Locate every uninfected red blood cell.
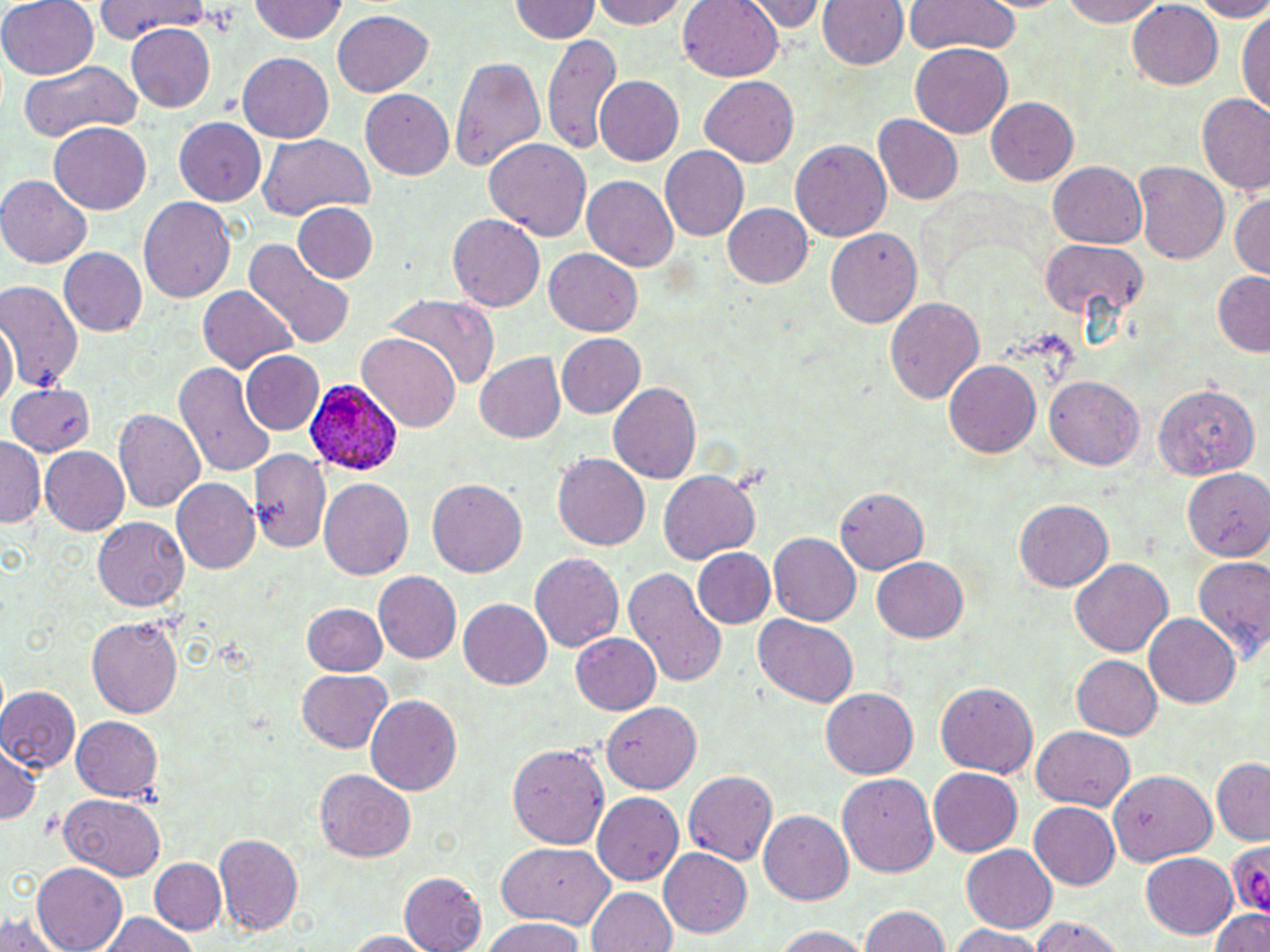

Approximate bounding boxes as (x1,y1)-(x2,y2) corner pairs in pixels.
Uninfected red blood cells: (1,0)-(99,79), (592,0)-(689,29), (678,0)-(783,81), (739,0)-(828,33), (818,0)-(907,69), (903,0)-(1020,56), (1062,0)-(1167,25), (1194,0)-(1270,21), (95,1)-(208,39), (248,1)-(349,42), (508,1)-(601,42), (1127,3)-(1223,88), (332,9)-(433,97), (1237,9)-(1269,115), (126,24)-(216,113), (544,31)-(620,155), (911,43)-(1012,137), (238,53)-(334,142), (450,54)-(545,172), (19,62)-(140,142), (596,75)-(684,165), (700,76)-(799,167), (361,89)-(453,179), (1197,93)-(1269,195), (986,97)-(1079,185), (873,114)-(963,205), (173,117)-(267,205), (50,122)-(151,213), (257,132)-(376,219), (484,138)-(590,240), (791,140)-(891,241), (659,145)-(748,242), (1048,161)-(1146,247), (1133,161)-(1228,264), (1,175)-(92,268), (582,175)-(678,271), (1230,193)-(1270,278), (138,196)-(235,302), (294,203)-(377,282), (723,204)-(813,288), (448,213)-(546,311), (825,228)-(923,328), (242,237)-(353,349), (1039,238)-(1147,319), (59,248)-(148,336), (545,249)-(642,337), (1212,269)-(1270,355), (0,279)-(85,395), (199,285)-(296,372), (382,294)-(499,388), (886,297)-(985,404), (0,318)-(18,405), (556,333)-(643,417), (358,334)-(460,430), (242,351)-(324,433), (474,351)-(566,442), (943,359)-(1041,457), (175,363)-(276,478), (1043,374)-(1144,470), (8,381)-(97,456), (1152,381)-(1260,480), (608,383)-(701,483), (113,408)-(206,512), (0,437)-(44,528), (39,444)-(129,536), (250,448)-(331,555), (552,454)-(650,550), (1179,467)-(1270,561), (658,469)-(761,564), (318,477)-(415,580), (171,478)-(260,575), (427,479)-(527,578), (835,488)-(928,574), (1014,500)-(1113,592), (92,516)-(190,612), (770,532)-(861,625), (693,548)-(775,628), (530,551)-(624,652), (871,555)-(968,643), (1192,556)-(1269,662), (1069,558)-(1174,657), (625,568)-(728,689), (373,569)-(461,664), (459,599)-(552,688), (303,602)-(386,675), (1144,613)-(1241,709), (754,615)-(857,707), (86,617)-(182,719), (571,632)-(660,714), (1071,654)-(1163,739), (298,670)-(392,752), (933,680)-(1041,778), (0,686)-(81,771), (820,688)-(918,777), (366,693)-(463,795), (603,701)-(701,794), (71,716)-(163,800), (1030,726)-(1135,811), (0,742)-(42,825), (506,742)-(611,849), (1211,758)-(1269,844), (929,767)-(1022,857), (316,769)-(416,862), (1109,769)-(1217,867), (683,770)-(778,866), (836,773)-(939,877), (592,790)-(684,884), (59,793)-(163,880), (1029,802)-(1119,889), (759,810)-(852,904), (214,832)-(305,935), (497,841)-(613,927), (961,844)-(1057,932), (659,847)-(752,939), (1140,853)-(1238,938), (150,857)-(227,934), (32,864)-(126,952), (399,872)-(487,952), (586,886)-(677,952), (859,905)-(950,952), (1210,910)-(1270,952), (98,913)-(198,952), (0,914)-(66,952), (1028,916)-(1128,952), (480,918)-(586,952), (948,925)-(1045,952), (770,926)-(872,951), (344,931)-(436,951).

{
  "slide_level_diagnosis": "Plasmodium ovale",
  "preparation": "thin blood smear",
  "image_size": "1270×952 pixels",
  "plasmodium_ovale_infected_red_blood_cell_locations": "approximate bounding boxes as (x1,y1)-(x2,y2) corner pairs in pixels: (303,378)-(403,473), (1227,844)-(1270,915)",
  "stain": "May-Grünwald-Giemsa",
  "field_of_view": "single",
  "platelet_locations": "approximate bounding boxes as (x1,y1)-(x2,y2) corner pairs in pixels: (197,4)-(242,37)",
  "modality": "optical microscopy",
  "magnification": "1000x"
}